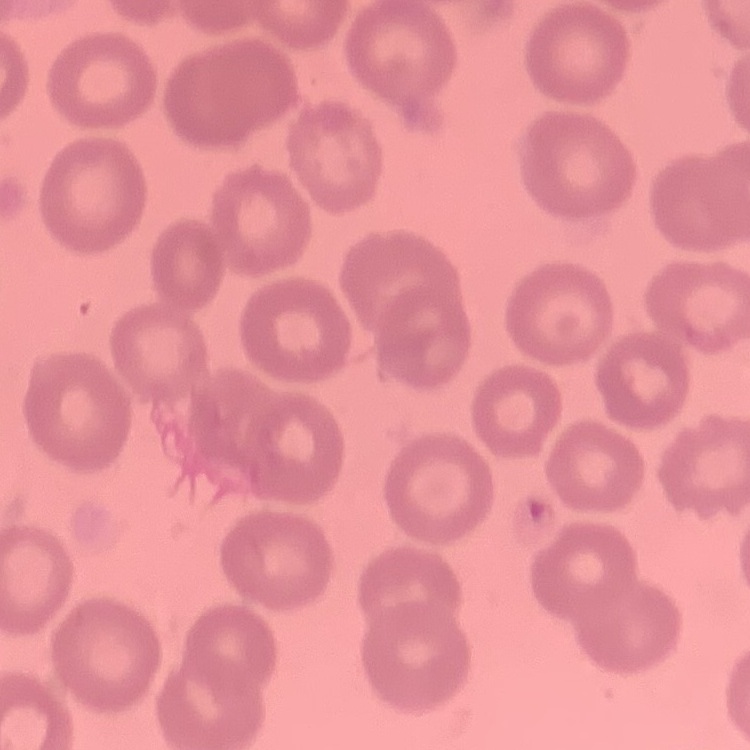
Summary:
  - Erythrocyte morphology: no rouleaux formation
  - Image type: one tile cut from a larger photomicrograph
  - Stain: Field's or Giemsa
  - Preparation: thin blood film